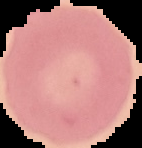

malaria_status: uninfected
image_type: segmented cell region on a black background
image_size: 142×148 pixels
preparation: thin blood smear